Report the malaria status of this cell.
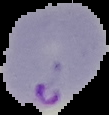

It is parasitized.

The area outside the segmented cell region is set to black. Image is 109×115 pixels. From a thin blood smear.